Comment on the morphology of the red blood cells.
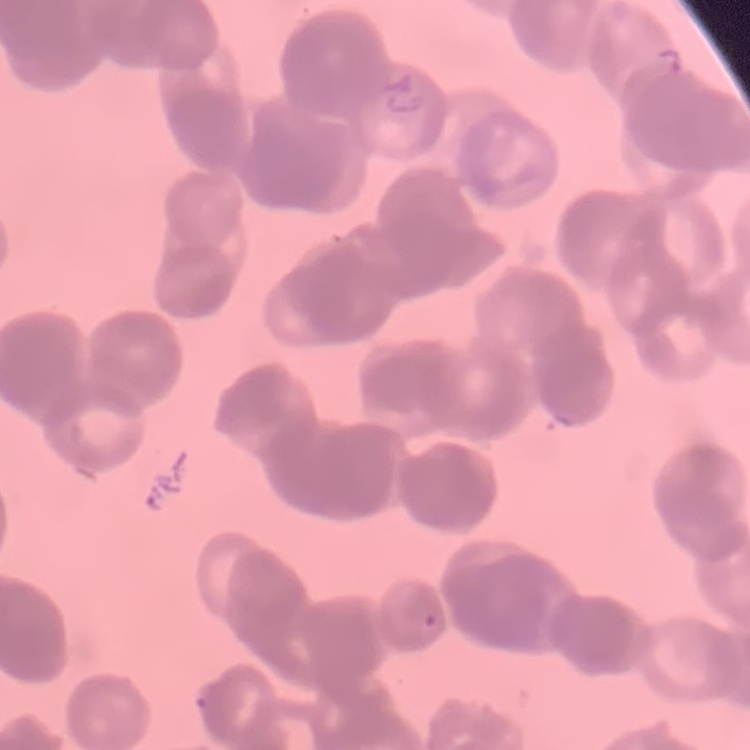

They show rouleaux formation.

Summary:
  - Image type: square crop of a larger photomicrograph
  - Preparation: thin peripheral smear
  - Stain: Field's or Giemsa